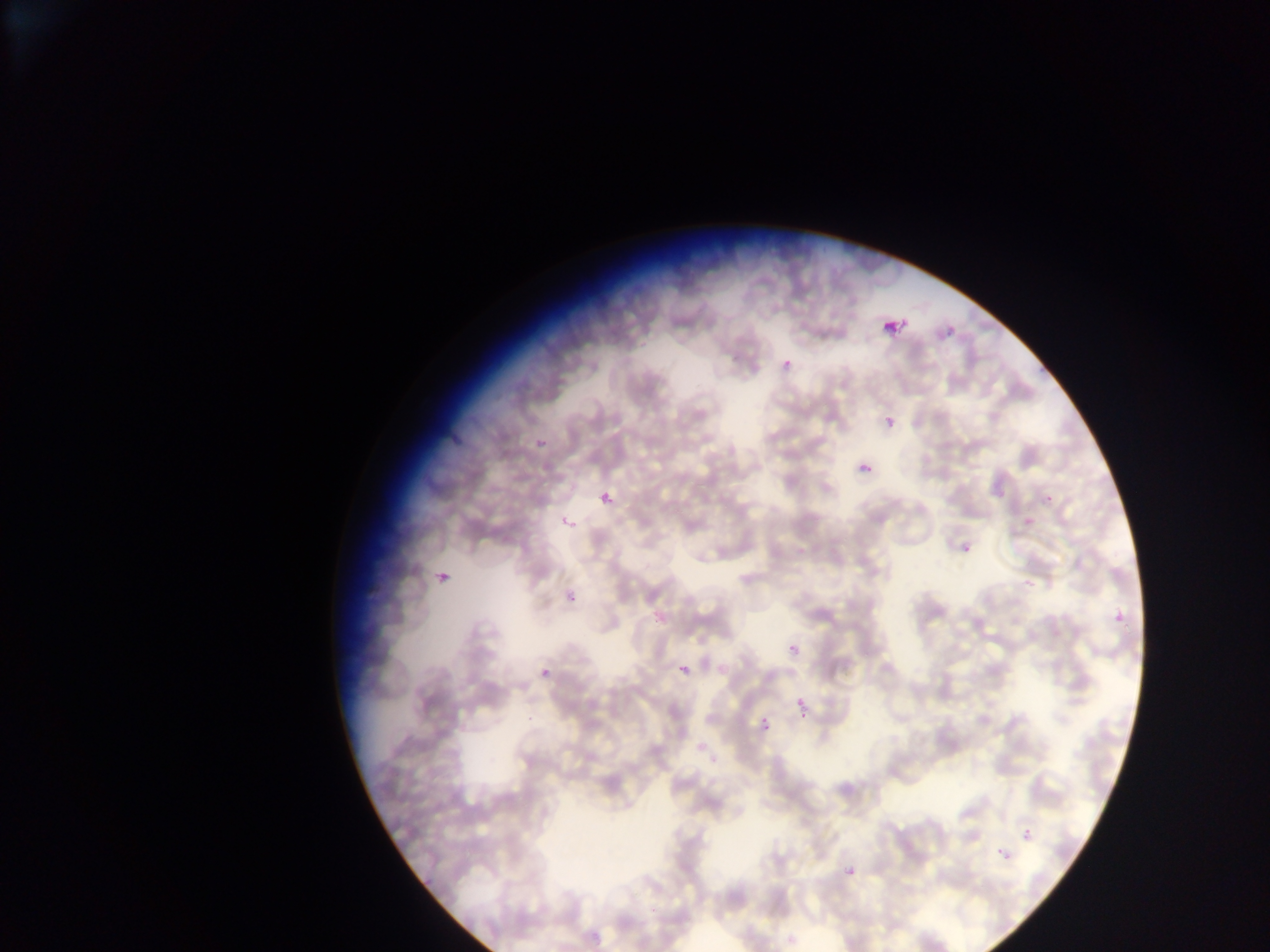

Approximate bounding boxes as [left, top, right, bottom] in pixels.
Summary:
  - Malaria parasite locations: [884, 318, 906, 338], [937, 326, 956, 344], [775, 347, 796, 370], [529, 414, 571, 450], [886, 418, 895, 428], [862, 464, 871, 474], [588, 486, 624, 518], [998, 491, 1007, 500], [1043, 493, 1054, 505], [557, 514, 582, 529], [1022, 520, 1040, 532], [955, 539, 978, 559], [430, 569, 448, 591], [1021, 569, 1041, 591], [567, 592, 577, 603], [1110, 609, 1126, 627], [651, 611, 666, 633], [788, 644, 798, 655], [675, 654, 701, 682], [540, 666, 555, 679], [795, 697, 804, 706], [525, 703, 544, 725], [800, 712, 808, 720], [760, 716, 771, 729], [1023, 829, 1032, 840], [994, 843, 1014, 867], [845, 866, 855, 875]
  - Capture: mobile-phone photograph through a microscope
  - Image size: 1270×952 pixels
  - Country: Ghana
  - Field of view: single
  - Preparation: thin blood film